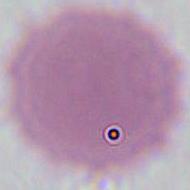
Summary:
  - Modality: photomicrograph
  - Magnification: 1000x
  - Identification: red blood cell